Give the position of every malaria parasite.
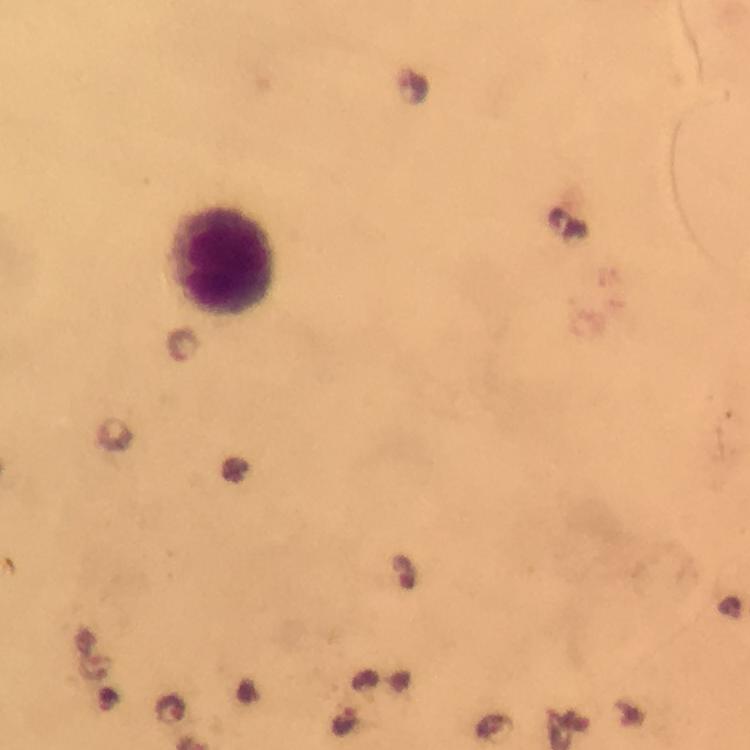
Approximate object centers, in pixels from the top-left corner.
Malaria parasites: (x=345, y=721).

preparation = thick smear
leukocyte locations = approximate object centers, in pixels from the top-left corner: (x=222, y=261)
capture = smartphone mounted on the microscope
cropped from = one field of view
immersion oil = used
image size = 750×750 pixels
stain = Giemsa
context = from a malaria diagnostic workup
magnification = 100x